Report the malaria status of this cell.
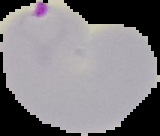
Parasitized.

Summary:
  - Preparation: thin blood film
  - Image size: 160×136 pixels
  - Image type: segmented cell region on a black background